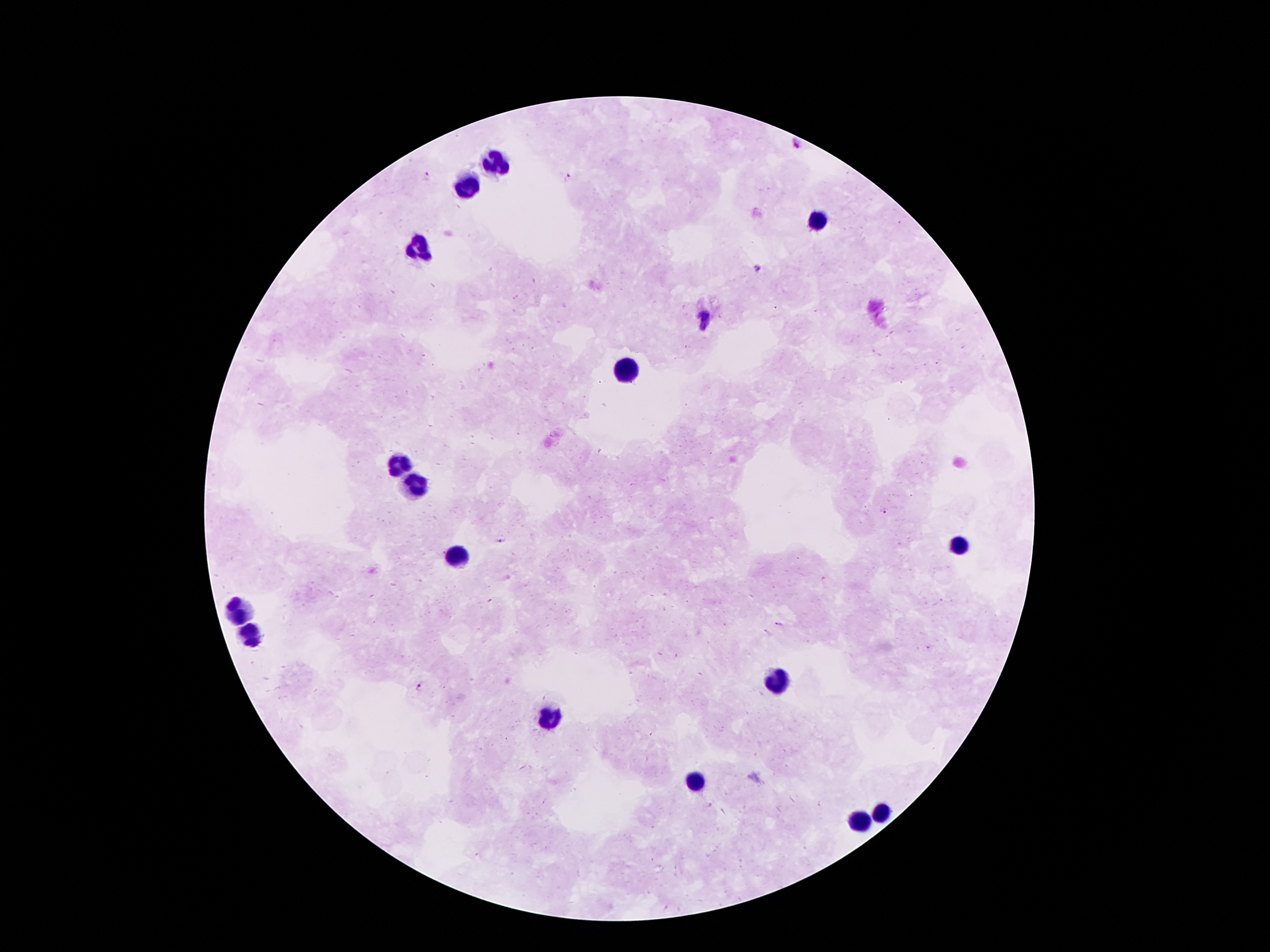 Patient malaria status: positive for Plasmodium falciparum. Smartphone photograph taken through the microscope eyepiece. Image is 1270×952 pixels. Single field of view. Giemsa-stained preparation. 100x magnification. Thick peripheral-blood smear.